Report the malaria status of this cell.
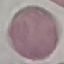

It is uninfected.

Giemsa stain. Acquired by smartphone through the microscope eyepiece. Thin blood smear. Automatically extracted cell patch, resized to 64 × 64 pixels.